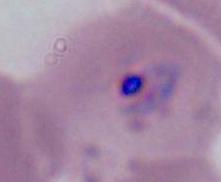

Summary:
  - Modality: micrograph
  - Magnification: 1000x
  - Identification: red blood cell